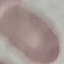
malaria_status: uninfected
capture: smartphone camera at the microscope eyepiece
stain: Giemsa
preparation: thin blood film
image_type: automatically extracted cell patch, resized to 64 × 64 pixels